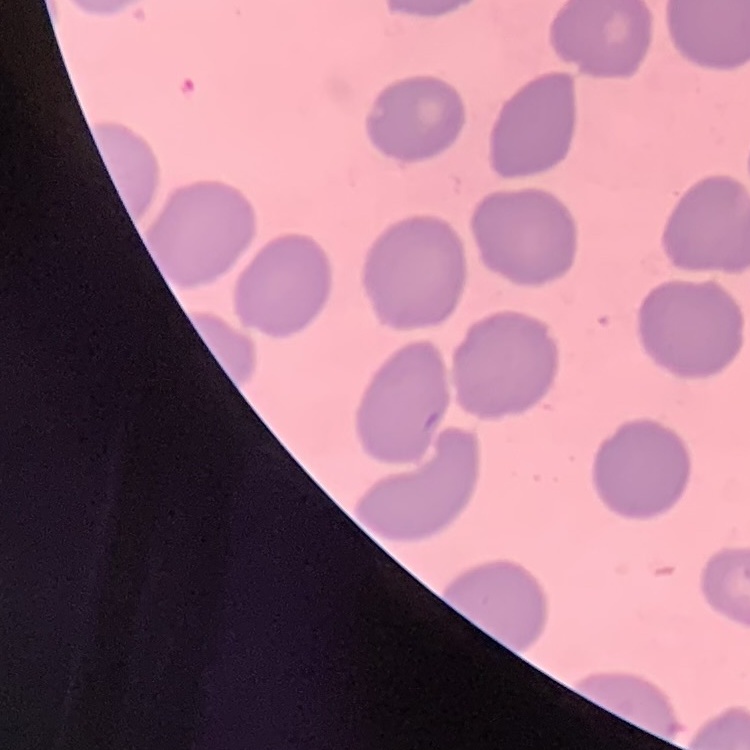
erythrocyte morphology = no rouleaux formation
image type = one tile cut from a larger photomicrograph
stain = Field's or Giemsa
preparation = thin peripheral smear